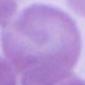
modality = photomicrograph
magnification = 1000x
identification = erythrocyte